Name the blood parasite species.
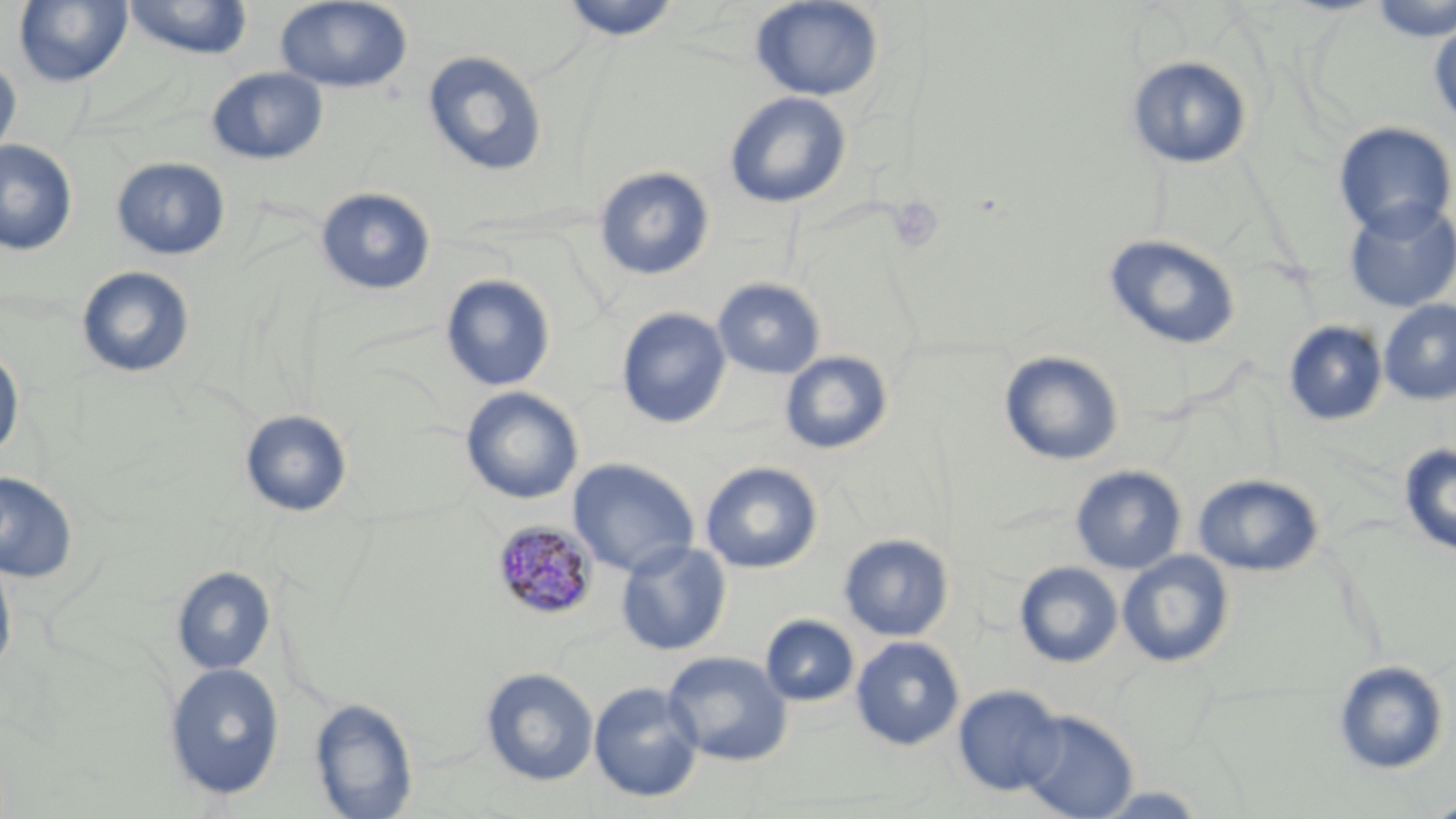
Plasmodium malariae.

preparation = thin blood film
modality = optical microscopy
uninfected red blood cell locations = approximate bounding boxes as (x1,y1)-(x2,y2) corner pairs in pixels: (13,0)-(133,87), (123,0)-(254,60), (275,0)-(413,94), (557,0)-(682,41), (750,0)-(884,101), (1366,0)-(1456,41), (1429,19)-(1456,128), (422,50)-(548,178), (1125,55)-(1254,170), (0,58)-(22,162), (206,67)-(328,164), (724,91)-(852,209), (1332,122)-(1455,239), (0,139)-(78,255), (111,157)-(230,260), (594,166)-(715,281), (315,187)-(436,296), (1343,199)-(1456,313), (1103,233)-(1242,350), (76,266)-(195,379), (440,274)-(556,392), (712,277)-(826,379), (1378,299)-(1456,405), (616,306)-(731,429), (1283,320)-(1388,427), (0,347)-(25,463), (999,350)-(1124,466), (779,351)-(893,456), (460,387)-(584,505), (240,409)-(353,517), (1399,444)-(1456,557), (568,458)-(700,578), (700,461)-(823,574), (1070,466)-(1186,574), (0,471)-(78,584), (1192,473)-(1324,577), (839,533)-(954,641), (616,541)-(732,656), (1117,550)-(1235,668), (0,554)-(17,677), (1015,561)-(1123,668), (172,566)-(276,675), (760,614)-(860,707), (850,636)-(965,751), (662,650)-(792,766), (1332,659)-(1450,775), (163,662)-(285,801), (480,667)-(599,786), (588,680)-(704,803), (953,684)-(1066,796), (309,697)-(419,818), (1018,709)-(1138,819), (1419,795)-(1456,818)
field of view = single
platelet locations = approximate bounding boxes as (x1,y1)-(x2,y2) corner pairs in pixels: (886,197)-(945,254)
Plasmodium malariae-infected red blood cell locations = approximate bounding boxes as (x1,y1)-(x2,y2) corner pairs in pixels: (491,521)-(598,621)
stain = May-Grünwald-Giemsa
magnification = 1000x
image size = 1456×819 pixels